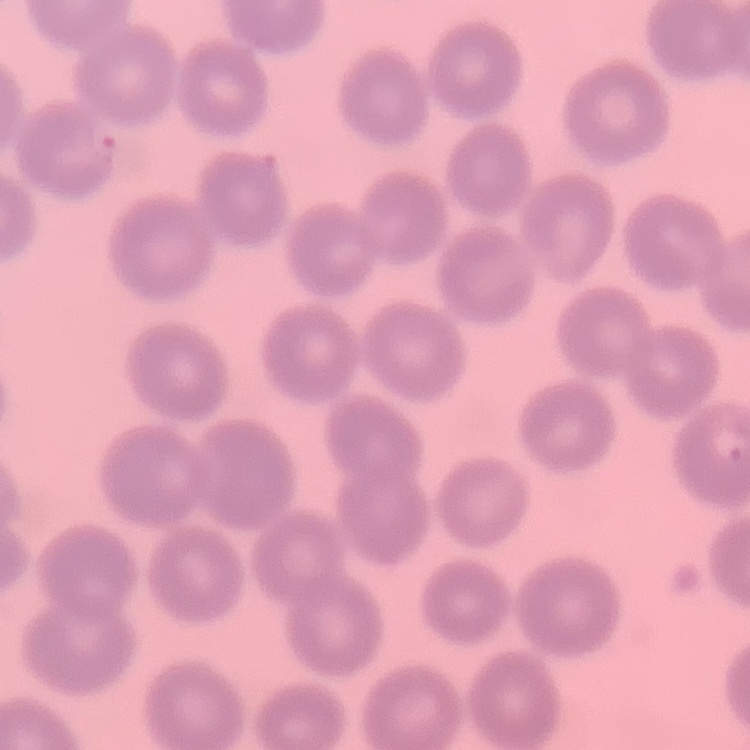
Summary:
  - Erythrocyte morphology: no rouleaux formation
  - Preparation: thin peripheral smear
  - Image type: one tile cut from a larger photomicrograph
  - Stain: Field's or Giemsa